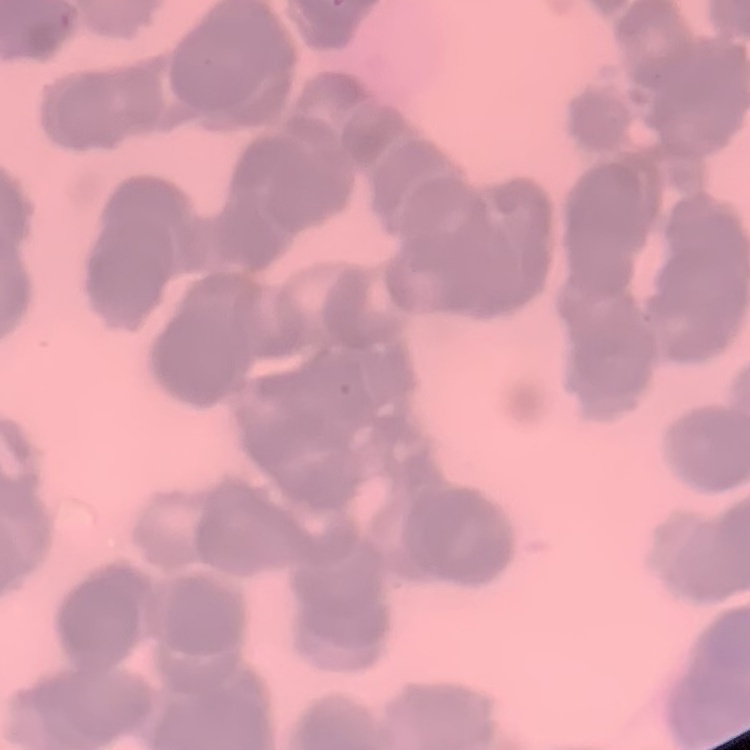

The red blood cells exhibit rouleaux formation. Square crop of a larger photomicrograph. Thin blood smear. Field's or Giemsa stain.